Identify the parasite.
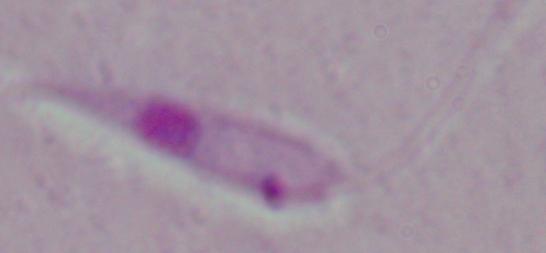
Leishmania.

Captured at 1000x magnification. Photomicrograph.